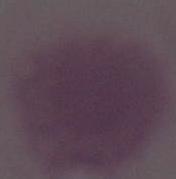
An erythrocyte is shown. Photomicrograph. 1000x magnification.